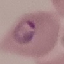 Result: malaria parasites identified. Giemsa-stained preparation. Thin smear of blood. Cell patch, automatically extracted from a larger field of view and resized to 64 × 64 pixels. Photographed with a smartphone camera at the microscope eyepiece.